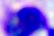
magnification = 400x
modality = micrograph
identification = leukocyte